Locate every Babesia divergens-infected red blood cell.
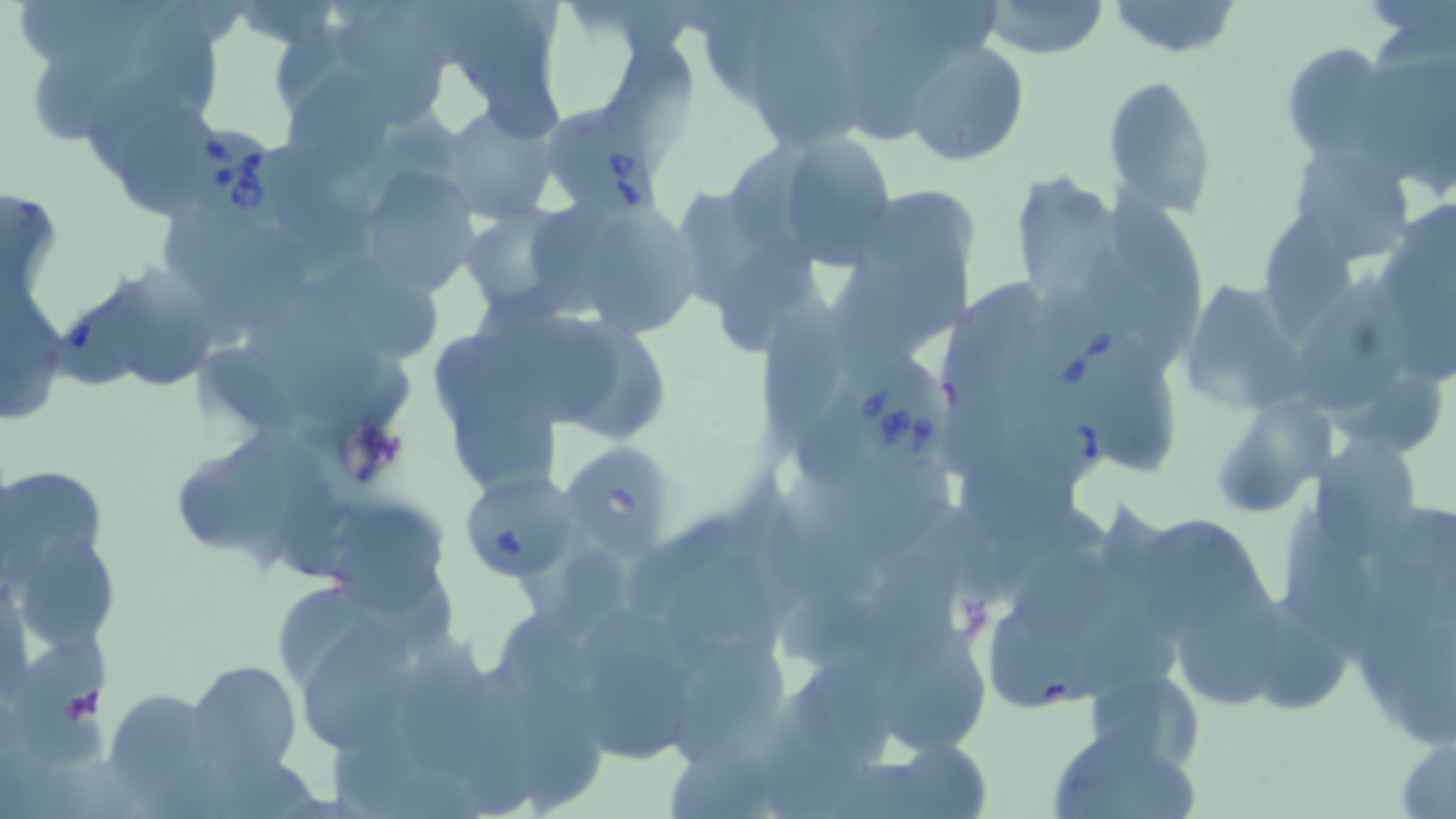

Approximate bounding boxes as named x1/y1/x2/y2 corners in pixels.
Babesia divergens-infected red blood cells: (x1=545, y1=104, x2=665, y2=218), (x1=184, y1=123, x2=290, y2=226), (x1=1029, y1=292, x2=1136, y2=401), (x1=847, y1=344, x2=956, y2=473).

Uninfected red blood cell locations: (x1=982, y1=0, x2=1110, y2=59), (x1=1107, y1=0, x2=1244, y2=58), (x1=754, y1=1, x2=854, y2=153), (x1=847, y1=5, x2=960, y2=143), (x1=907, y1=39, x2=1031, y2=168), (x1=1280, y1=41, x2=1398, y2=163), (x1=290, y1=68, x2=392, y2=193), (x1=1103, y1=73, x2=1218, y2=219), (x1=439, y1=104, x2=559, y2=225), (x1=119, y1=108, x2=216, y2=222), (x1=767, y1=128, x2=898, y2=264), (x1=1289, y1=142, x2=1416, y2=265), (x1=363, y1=166, x2=479, y2=292), (x1=1005, y1=169, x2=1124, y2=309), (x1=1110, y1=191, x2=1209, y2=348), (x1=461, y1=205, x2=571, y2=312), (x1=1258, y1=206, x2=1369, y2=345), (x1=591, y1=214, x2=704, y2=338), (x1=720, y1=234, x2=826, y2=353), (x1=116, y1=260, x2=215, y2=388), (x1=298, y1=263, x2=442, y2=363), (x1=1300, y1=264, x2=1410, y2=418), (x1=1178, y1=272, x2=1327, y2=409), (x1=2, y1=293, x2=67, y2=426), (x1=760, y1=295, x2=855, y2=460), (x1=495, y1=316, x2=628, y2=428), (x1=1094, y1=349, x2=1171, y2=477), (x1=456, y1=380, x2=569, y2=487), (x1=1213, y1=410, x2=1317, y2=518), (x1=961, y1=432, x2=1087, y2=546), (x1=1313, y1=436, x2=1423, y2=551), (x1=179, y1=437, x2=295, y2=556), (x1=556, y1=441, x2=671, y2=550), (x1=0, y1=464, x2=110, y2=572), (x1=457, y1=470, x2=578, y2=583), (x1=768, y1=470, x2=898, y2=606), (x1=1281, y1=507, x2=1387, y2=677), (x1=337, y1=509, x2=448, y2=609), (x1=1145, y1=510, x2=1269, y2=643), (x1=9, y1=528, x2=120, y2=659), (x1=1348, y1=536, x2=1456, y2=748), (x1=1016, y1=545, x2=1124, y2=646), (x1=668, y1=547, x2=786, y2=672), (x1=1179, y1=552, x2=1291, y2=713), (x1=285, y1=590, x2=385, y2=683), (x1=1259, y1=598, x2=1353, y2=713), (x1=890, y1=621, x2=990, y2=752), (x1=305, y1=624, x2=416, y2=754), (x1=411, y1=631, x2=497, y2=778), (x1=16, y1=641, x2=114, y2=766), (x1=674, y1=642, x2=791, y2=772), (x1=589, y1=646, x2=698, y2=765), (x1=186, y1=657, x2=302, y2=776), (x1=516, y1=662, x2=604, y2=819), (x1=1087, y1=679, x2=1202, y2=773), (x1=117, y1=689, x2=219, y2=815), (x1=1046, y1=725, x2=1199, y2=819), (x1=1391, y1=726, x2=1456, y2=817), (x1=869, y1=737, x2=996, y2=819). Platelet locations: (x1=338, y1=416, x2=413, y2=488), (x1=58, y1=685, x2=103, y2=726). Slide-level diagnosis: Babesia divergens. Single field of view. Light microscopy. Image is 1456×819 pixels. Thin blood film. 1000x magnification. May-Grünwald-Giemsa stain.